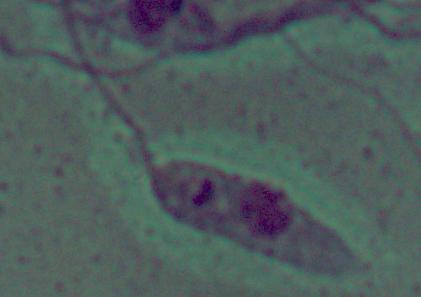 Captured at 1000x magnification. A Leishmania parasite is seen. Micrograph.